Assess this cell for malaria.
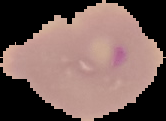
It is parasitized.

Summary:
  - Image type: segmented cell region on a black background
  - Preparation: thin blood film
  - Image size: 166×121 pixels